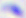 Photomicrograph. 400x magnification. Toxoplasma gondii is shown.